Assess this cell for malaria.
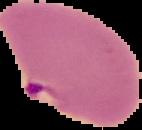

Parasitized.

Image is 142×130 pixels. Cell region segmented out of the field of view; the surrounding area is masked to black. From a thin blood film.